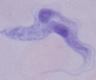
{
  "identification": "trypanosome",
  "modality": "photomicrograph",
  "magnification": "1000x"
}